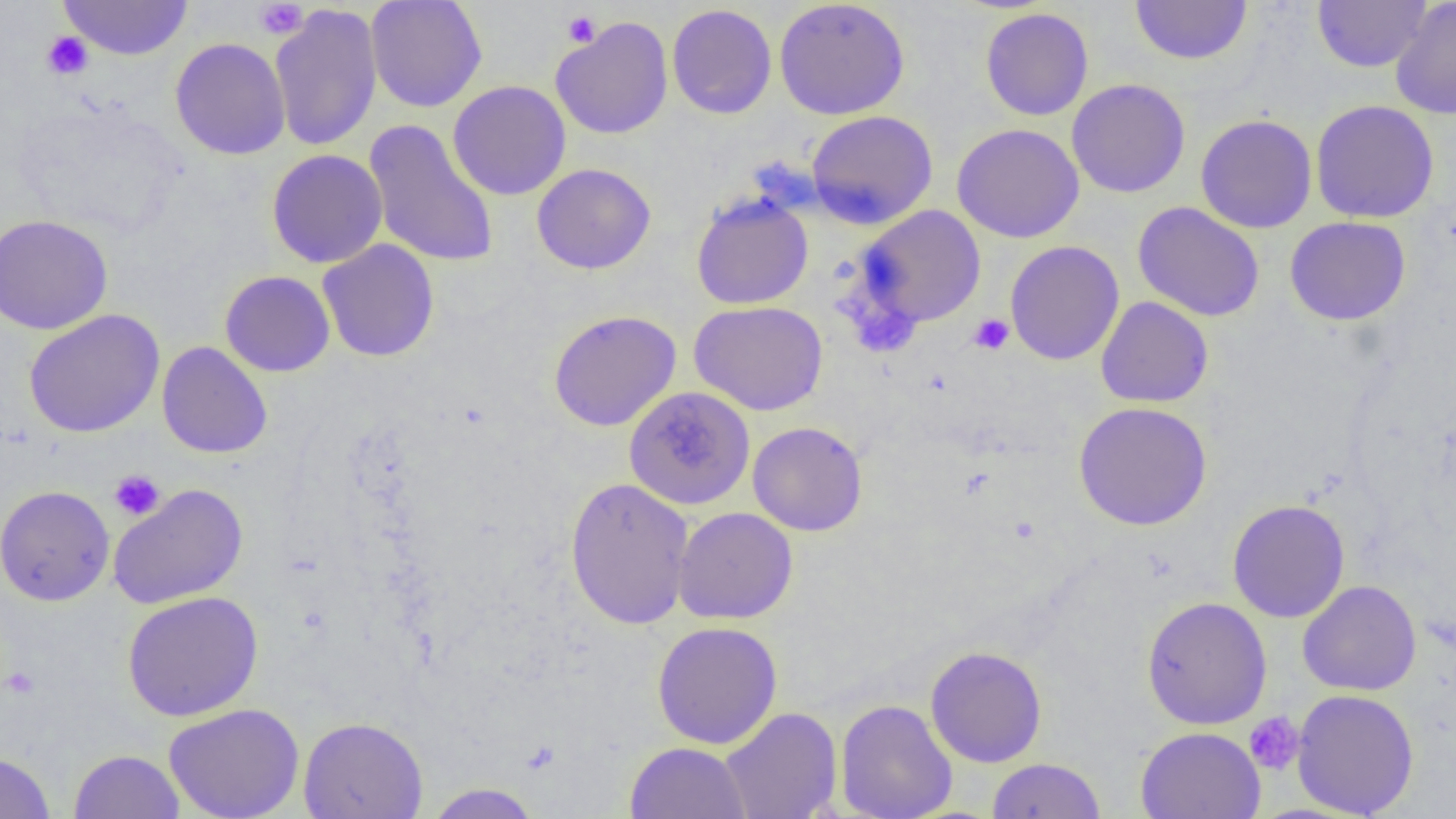

slide-level diagnosis = no evidence of blood parasites
image size = 1456×819 pixels
magnification = 1000x
modality = optical microscopy
uninfected red blood cell locations = approximate bounding boxes as (x1, y1, x2, y2) in pixels: (58, 0, 194, 61), (365, 0, 488, 113), (774, 0, 910, 120), (1313, 0, 1431, 73), (1390, 0, 1456, 119), (1130, 1, 1252, 65), (268, 3, 383, 153), (667, 4, 777, 119), (979, 8, 1094, 121), (551, 16, 674, 140), (170, 38, 291, 160), (1066, 78, 1190, 198), (447, 80, 571, 200), (1310, 100, 1440, 223), (806, 110, 938, 228), (1195, 114, 1318, 233), (364, 119, 500, 269), (951, 123, 1084, 243), (267, 149, 388, 268), (532, 163, 657, 275), (690, 193, 814, 310), (1133, 202, 1265, 322), (857, 204, 986, 329), (0, 213, 114, 335), (1285, 216, 1411, 326), (317, 239, 440, 363), (1005, 240, 1124, 365), (220, 270, 335, 377), (1096, 296, 1213, 408), (689, 301, 828, 416), (23, 309, 164, 438), (548, 310, 681, 432), (157, 341, 272, 459), (624, 386, 755, 510), (1073, 401, 1213, 530), (748, 421, 867, 537), (564, 477, 695, 630), (108, 483, 248, 610), (0, 485, 115, 606), (1227, 499, 1350, 623), (673, 507, 799, 624), (1298, 579, 1422, 696), (122, 591, 263, 722), (1141, 596, 1272, 730), (652, 621, 783, 749), (925, 646, 1048, 768), (1292, 688, 1420, 817), (835, 699, 957, 819), (164, 703, 304, 819), (720, 707, 842, 819), (298, 715, 428, 819), (1136, 726, 1265, 819), (624, 742, 752, 818), (68, 749, 186, 818), (0, 751, 56, 818), (987, 758, 1105, 818), (423, 782, 543, 818)
platelet locations = approximate bounding boxes as (x1, y1, x2, y2) in pixels: (255, 1, 309, 39), (561, 10, 601, 48), (42, 31, 93, 80), (969, 313, 1014, 355), (108, 469, 166, 521), (1, 666, 41, 699), (1244, 712, 1305, 775)
preparation = thin blood smear
field of view = single